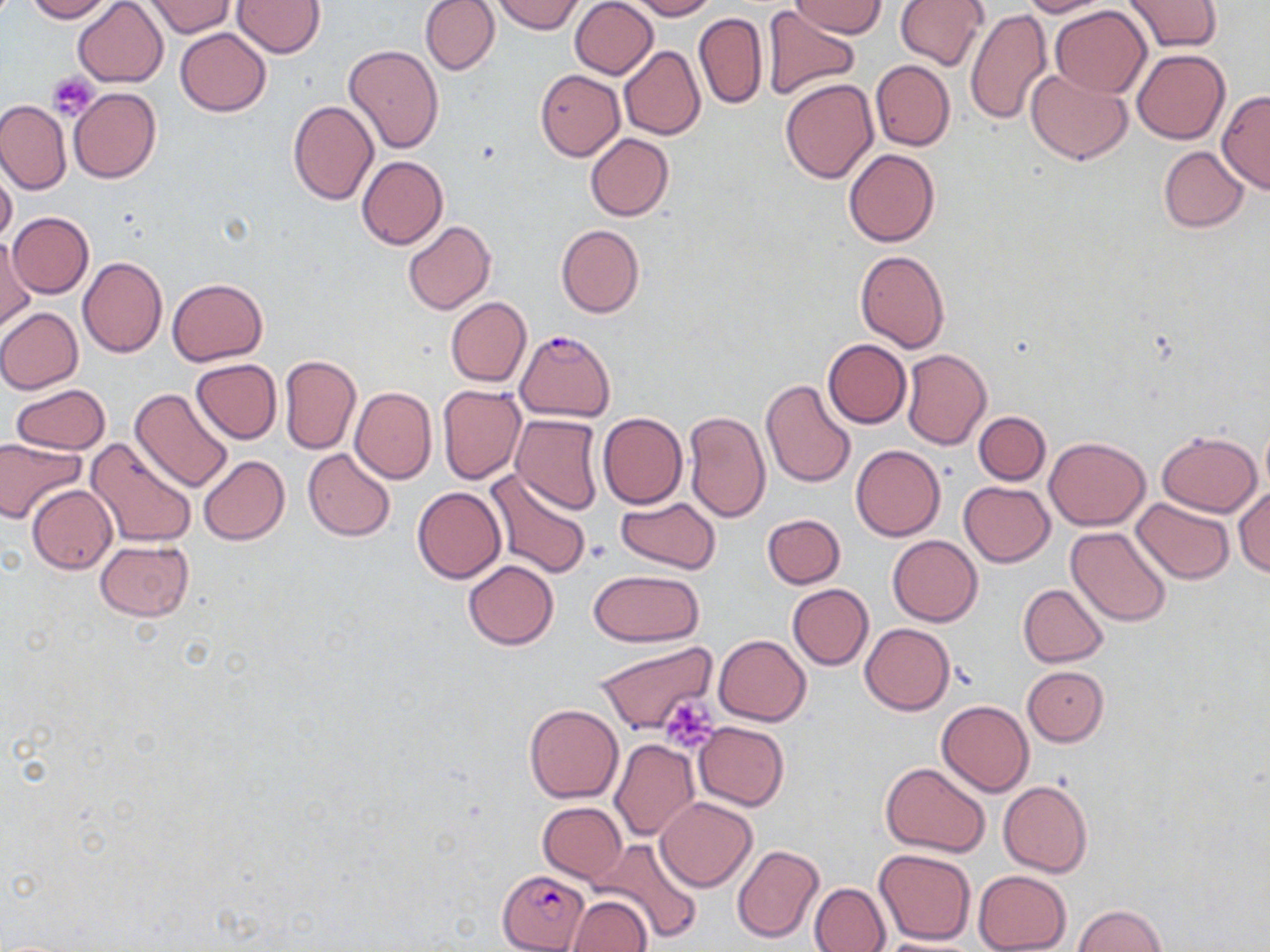
Summary:
  - Coordinate format: approximate bounding boxes as (x1, y1, x2, y2) in pixels
  - Uninfected red blood cell locations: (24, 0, 113, 22), (73, 0, 169, 86), (233, 0, 325, 57), (420, 0, 499, 75), (495, 0, 583, 35), (569, 0, 658, 79), (629, 0, 716, 20), (790, 0, 888, 38), (895, 0, 990, 71), (1019, 0, 1109, 17), (144, 1, 235, 37), (1122, 1, 1222, 53), (1050, 6, 1151, 98), (760, 7, 861, 101), (965, 8, 1052, 128), (694, 12, 767, 109), (175, 28, 271, 116), (344, 44, 444, 153), (619, 46, 705, 140), (1133, 49, 1229, 144), (869, 59, 955, 151), (1025, 68, 1131, 165), (534, 70, 625, 160), (780, 78, 880, 184), (69, 87, 161, 183), (1216, 91, 1270, 194), (0, 98, 71, 194), (288, 100, 378, 205), (585, 134, 674, 220), (1158, 145, 1248, 231), (844, 148, 941, 247), (356, 156, 448, 249), (0, 166, 17, 247), (9, 212, 93, 297), (403, 220, 495, 314), (557, 223, 644, 318), (1, 234, 34, 334), (854, 250, 950, 353), (78, 256, 167, 357), (168, 278, 267, 366), (446, 297, 530, 387), (0, 308, 82, 393), (822, 339, 912, 428), (901, 349, 992, 451), (279, 355, 361, 455), (190, 359, 281, 444), (760, 379, 856, 488), (9, 383, 110, 455), (437, 385, 525, 483), (350, 386, 436, 484), (130, 387, 234, 493), (681, 409, 770, 523), (597, 412, 686, 509), (974, 412, 1050, 484), (510, 413, 605, 514), (1259, 419, 1270, 500), (1156, 430, 1263, 516), (0, 436, 82, 524), (87, 437, 197, 549), (1045, 437, 1151, 530), (851, 445, 944, 541), (303, 448, 395, 542), (198, 455, 290, 545), (483, 470, 593, 581), (958, 481, 1054, 566), (27, 485, 117, 573), (412, 486, 506, 583), (1234, 486, 1270, 576), (616, 497, 721, 575), (1131, 498, 1235, 584), (762, 513, 846, 589), (1066, 526, 1172, 627), (887, 534, 982, 626), (95, 540, 194, 621), (463, 561, 558, 650), (588, 570, 703, 645), (787, 584, 873, 669), (1017, 584, 1109, 667), (860, 623, 955, 714), (715, 634, 810, 725), (594, 640, 719, 735), (1022, 666, 1109, 746), (936, 701, 1033, 796), (524, 704, 623, 803), (693, 721, 789, 810), (610, 739, 699, 842), (881, 762, 991, 858), (998, 779, 1093, 877), (656, 797, 757, 892), (537, 802, 626, 884), (592, 837, 703, 946), (732, 843, 824, 943), (874, 848, 977, 945), (972, 870, 1072, 952), (809, 882, 891, 951), (564, 895, 652, 952), (1072, 905, 1168, 951), (872, 937, 985, 952)
  - Plasmodium falciparum-infected red blood cell locations: (514, 329, 615, 421), (498, 870, 592, 951)
  - Platelet locations: (46, 72, 100, 121), (661, 697, 718, 753)
  - Slide-level diagnosis: Plasmodium falciparum
  - Preparation: thin blood smear
  - Field of view: single
  - Image size: 1270×952 pixels
  - Stain: May-Grünwald-Giemsa
  - Magnification: 1000x
  - Modality: optical microscopy